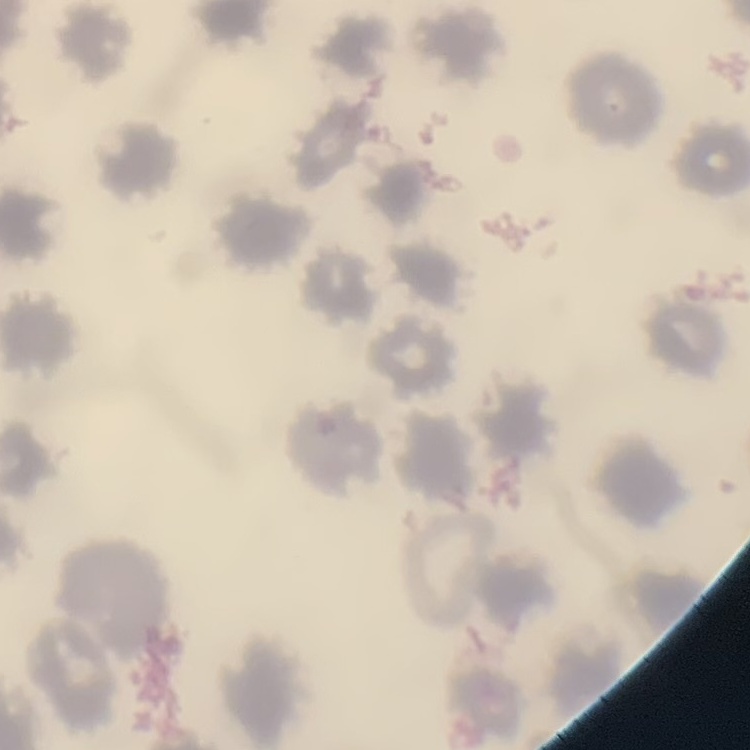

The red blood cells show no rouleaux formation. Thin blood smear. Square crop of a larger photomicrograph. Stained with either Field's or Giemsa.